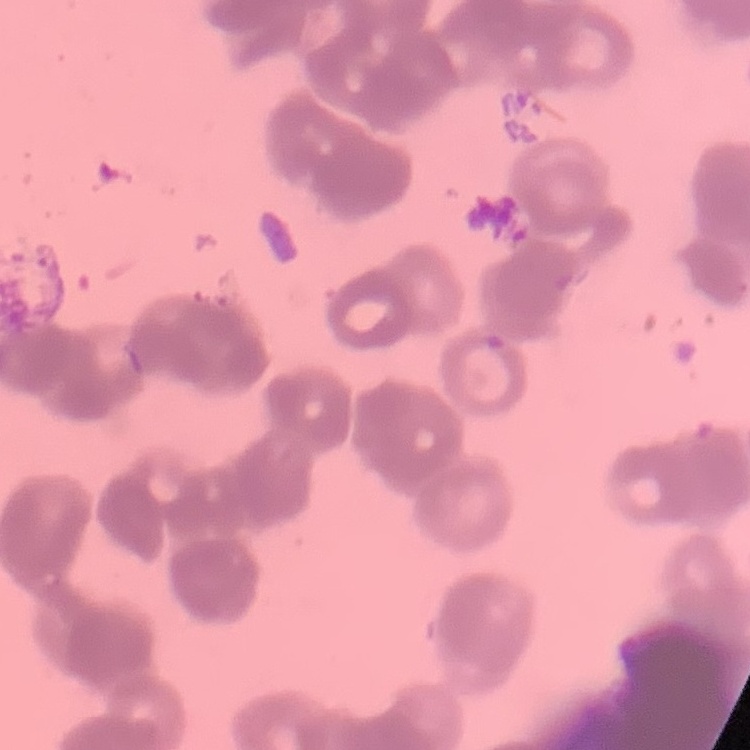
Summary:
  - Erythrocyte morphology: rouleaux formation
  - Stain: Field's or Giemsa
  - Image type: square crop of a larger photomicrograph
  - Preparation: thin blood film